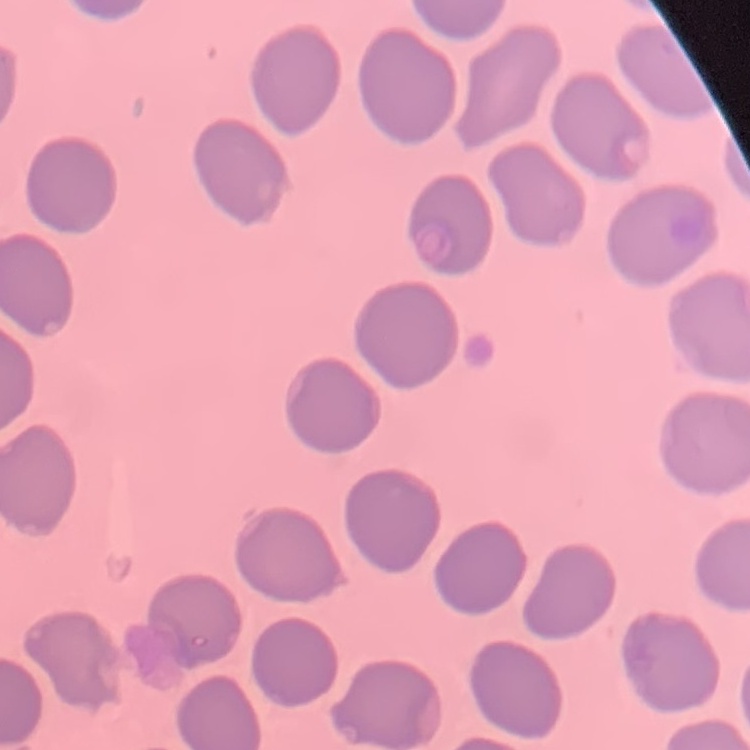

{
  "erythrocyte_morphology": "no rouleaux formation",
  "image_type": "square crop of a larger photomicrograph",
  "preparation": "thin blood smear",
  "stain": "Field's or Giemsa"
}